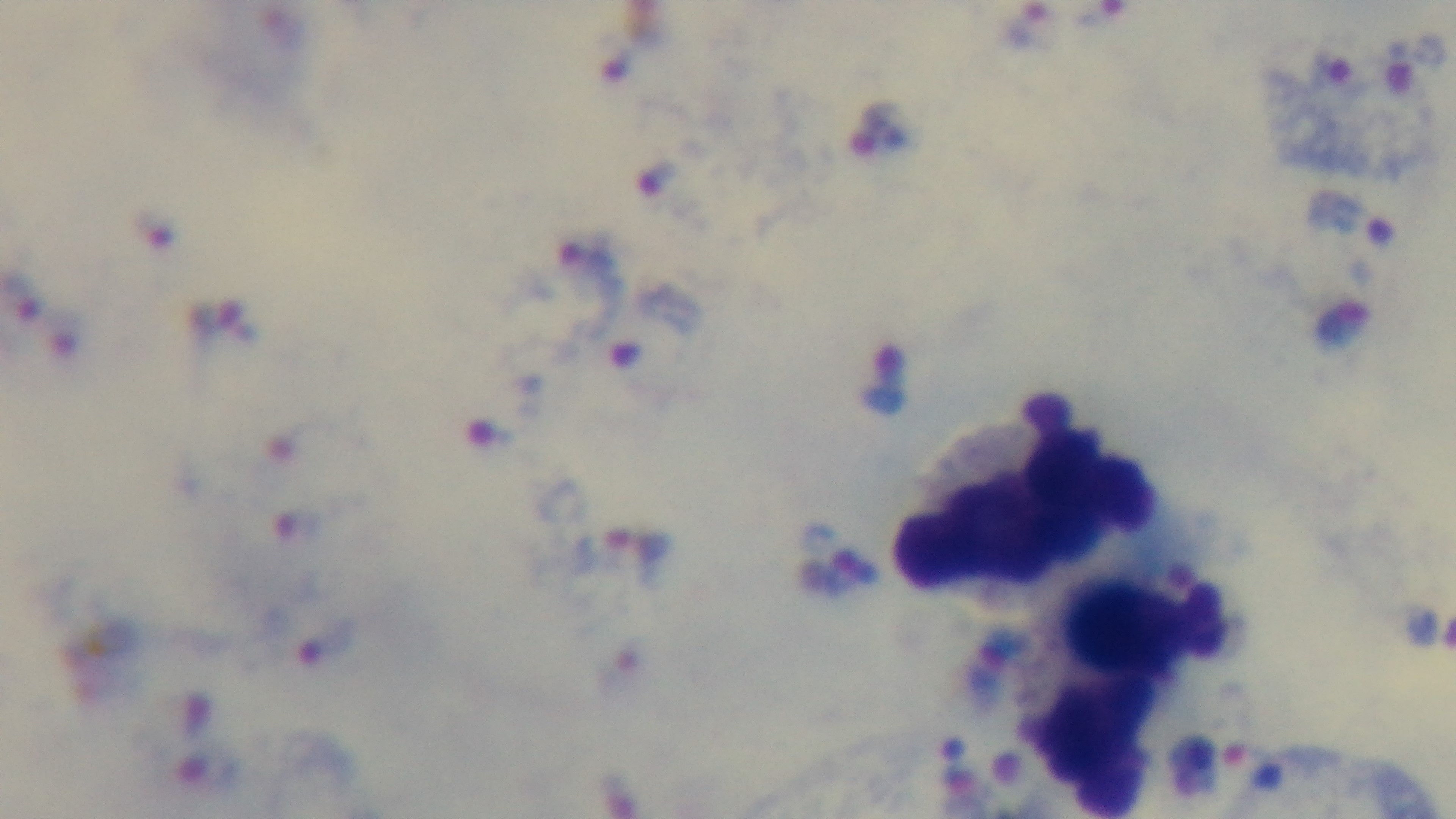

Summary:
  - Modality: light microscopy
  - Objective: 100x oil immersion
  - Malaria status: infected
  - Capture: mounted 4K digital camera
  - Stain: Giemsa
  - Preparation: thick smear
  - Field of view: single